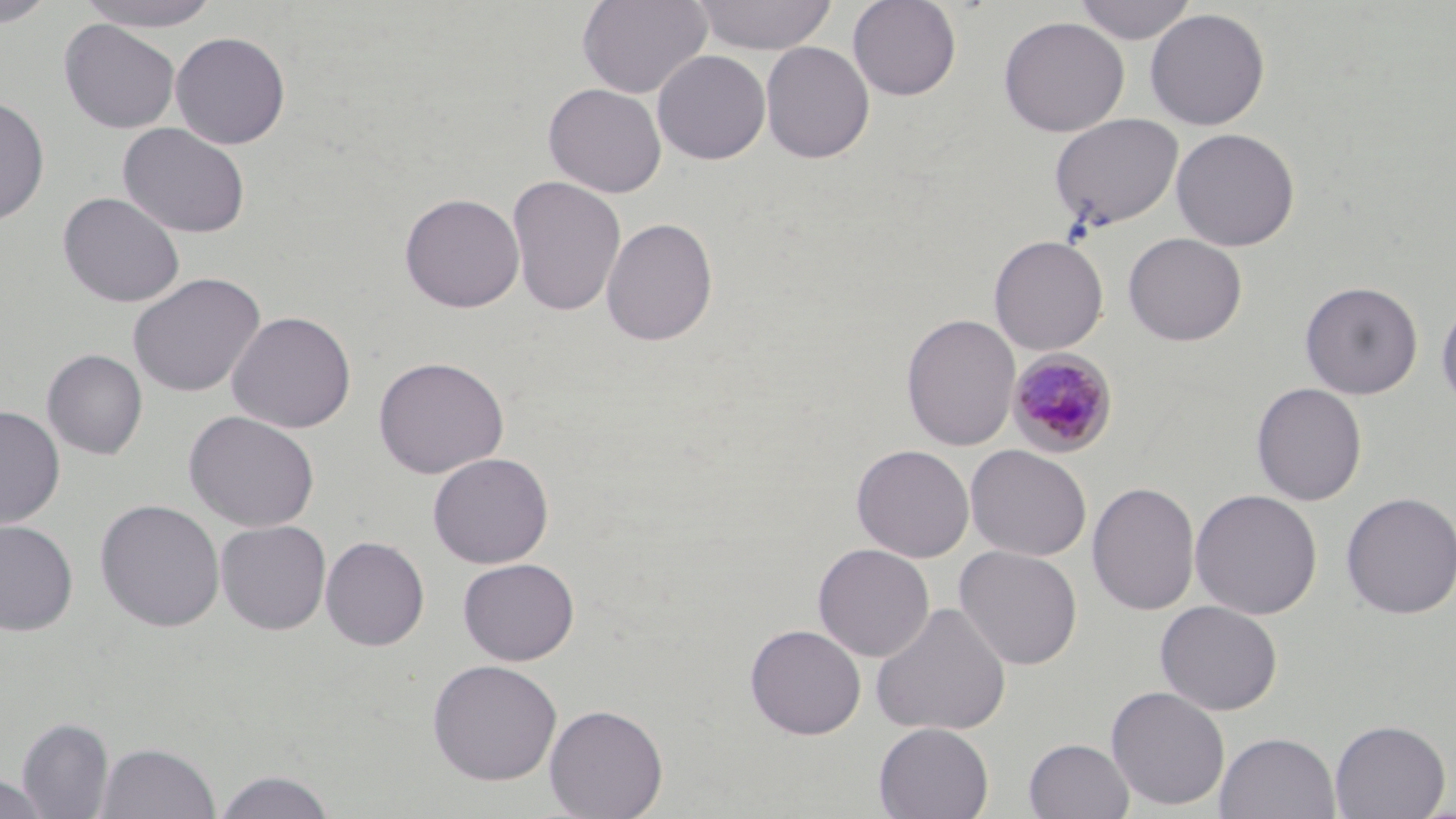 Approximate bounding boxes as named x1/y1/x2/y2 corners in pixels. Plasmodium malariae-infected red blood cell locations: (x1=1007, y1=349, x2=1119, y2=458). Uninfected red blood cell locations: (x1=0, y1=0, x2=58, y2=27), (x1=74, y1=0, x2=221, y2=32), (x1=577, y1=0, x2=712, y2=99), (x1=690, y1=0, x2=839, y2=54), (x1=847, y1=0, x2=962, y2=100), (x1=1073, y1=0, x2=1197, y2=44), (x1=1144, y1=8, x2=1271, y2=130), (x1=999, y1=16, x2=1129, y2=137), (x1=59, y1=19, x2=180, y2=133), (x1=170, y1=31, x2=291, y2=149), (x1=760, y1=41, x2=875, y2=164), (x1=652, y1=50, x2=771, y2=164), (x1=543, y1=83, x2=666, y2=198), (x1=0, y1=95, x2=50, y2=226), (x1=1049, y1=114, x2=1183, y2=231), (x1=116, y1=122, x2=251, y2=239), (x1=1171, y1=127, x2=1300, y2=251), (x1=506, y1=175, x2=626, y2=317), (x1=57, y1=191, x2=185, y2=307), (x1=399, y1=192, x2=525, y2=313), (x1=601, y1=216, x2=719, y2=347), (x1=1122, y1=232, x2=1247, y2=346), (x1=989, y1=234, x2=1108, y2=356), (x1=128, y1=272, x2=266, y2=397), (x1=1300, y1=280, x2=1423, y2=399), (x1=1436, y1=295, x2=1456, y2=412), (x1=226, y1=310, x2=357, y2=434), (x1=901, y1=313, x2=1021, y2=451), (x1=42, y1=349, x2=148, y2=460), (x1=372, y1=355, x2=509, y2=479), (x1=1251, y1=382, x2=1367, y2=506), (x1=0, y1=405, x2=65, y2=528), (x1=183, y1=409, x2=320, y2=533), (x1=852, y1=444, x2=974, y2=562), (x1=965, y1=444, x2=1092, y2=561), (x1=427, y1=452, x2=554, y2=568), (x1=1087, y1=481, x2=1200, y2=616), (x1=1190, y1=488, x2=1323, y2=619), (x1=1340, y1=491, x2=1456, y2=619), (x1=94, y1=498, x2=225, y2=632), (x1=0, y1=519, x2=79, y2=636), (x1=215, y1=519, x2=331, y2=635), (x1=320, y1=536, x2=430, y2=651), (x1=813, y1=543, x2=935, y2=662), (x1=953, y1=546, x2=1083, y2=670), (x1=457, y1=557, x2=580, y2=666), (x1=1155, y1=600, x2=1282, y2=715), (x1=870, y1=601, x2=1012, y2=737), (x1=745, y1=623, x2=866, y2=739), (x1=426, y1=658, x2=563, y2=785), (x1=1105, y1=686, x2=1230, y2=811), (x1=544, y1=703, x2=668, y2=819), (x1=17, y1=716, x2=114, y2=818), (x1=1329, y1=719, x2=1451, y2=819), (x1=873, y1=722, x2=994, y2=819), (x1=1214, y1=731, x2=1340, y2=819), (x1=1023, y1=738, x2=1134, y2=819), (x1=96, y1=741, x2=221, y2=818), (x1=211, y1=768, x2=339, y2=818), (x1=1, y1=772, x2=51, y2=819). Slide-level diagnosis: Plasmodium malariae. Captured at 1000x magnification. Thin blood smear. Single field of view. May-Grünwald-Giemsa-stained preparation. Image is 1456×819 pixels. Light microscopy.